Classify this cell by malaria status.
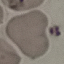

Uninfected.

Cell patch, automatically extracted from a larger field of view and resized to 64 × 64 pixels. Thin smear of blood. Giemsa-stained preparation. Photographed with a smartphone camera at the microscope eyepiece.